Describe the morphology of the red blood cells.
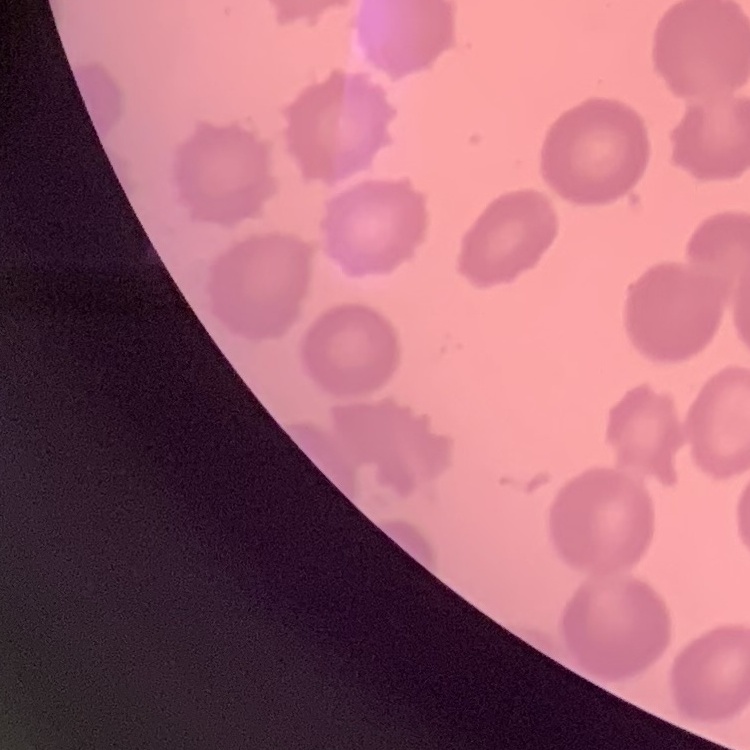
No rouleaux formation.

Thin blood film. Stained with either Field's or Giemsa. Square crop of a larger photomicrograph.